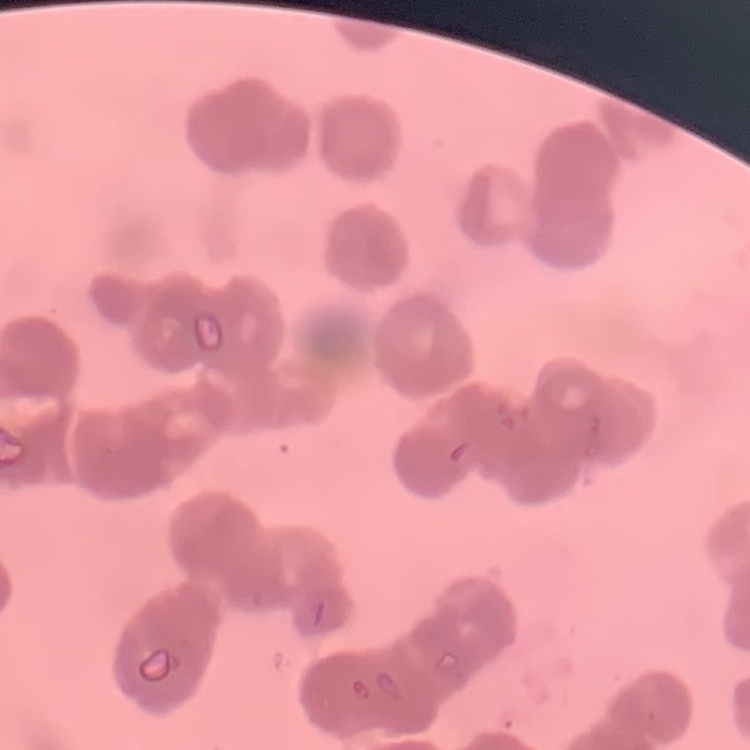

erythrocyte morphology = rouleaux formation
preparation = thin blood film
image type = one tile cut from a larger photomicrograph
stain = Field's or Giemsa